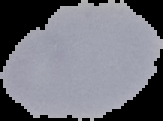

Summary:
  - Image size: 163×121 pixels
  - Malaria status: uninfected
  - Image type: segmented cell region on a black background
  - Preparation: thin blood film